Point out each Plasmodium parasite.
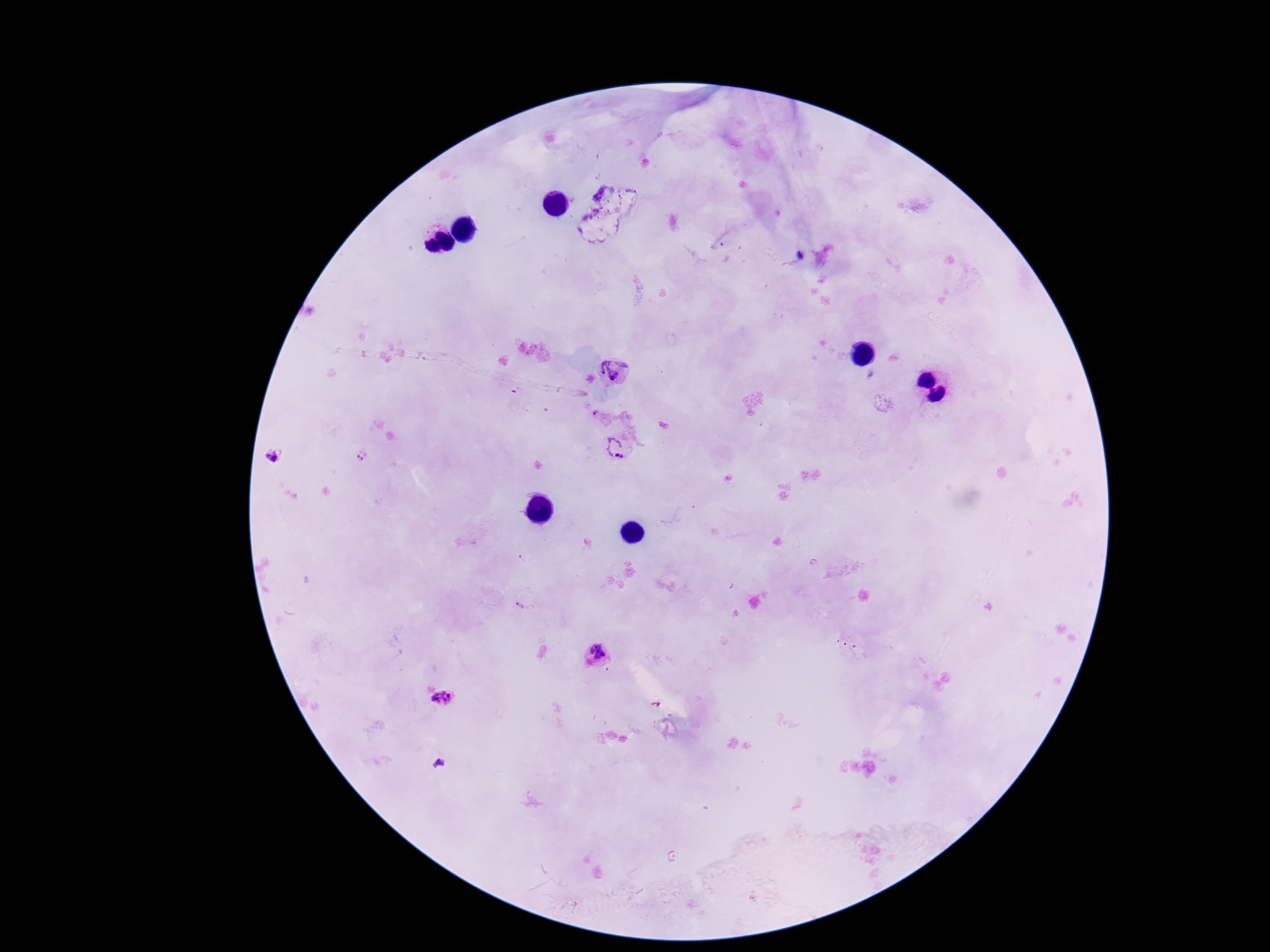

Approximate centers as (x, y) in pixels.
Plasmodium parasites: (615, 368), (595, 413), (614, 446), (363, 454), (276, 458), (520, 605), (597, 655), (443, 697).

Patient malaria status: infected. Image is 1270×952 pixels. Single field of view. Photographed through the microscope eyepiece with a smartphone camera. 100x magnification. Thick peripheral-blood smear. Giemsa-stained preparation.